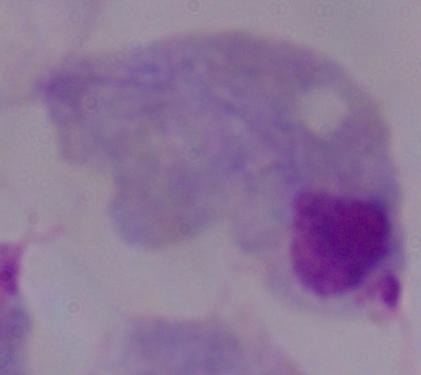
Summary:
  - Identification: trichomonad
  - Modality: photomicrograph
  - Magnification: 1000x